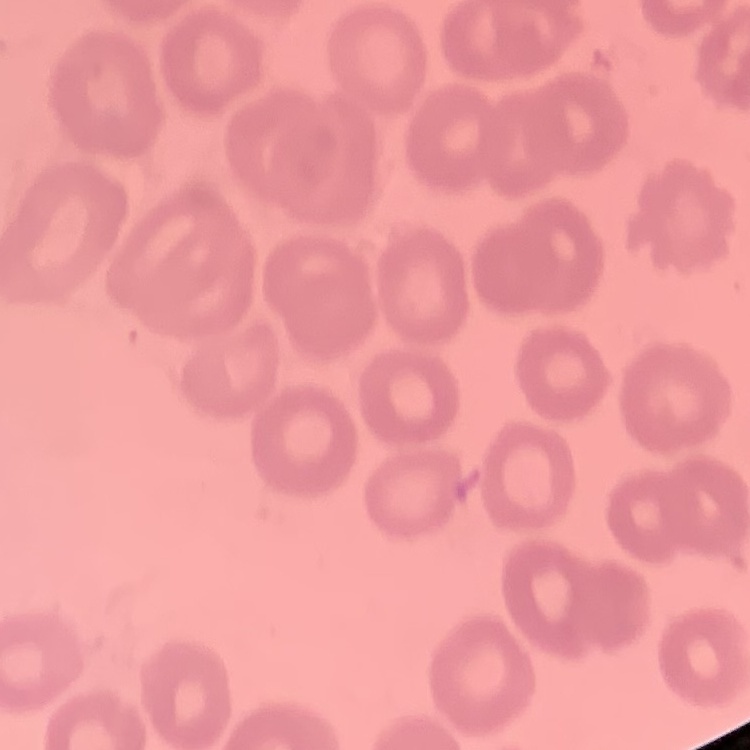
Summary:
  - Erythrocyte morphology: no rouleaux formation
  - Stain: Field's or Giemsa
  - Preparation: thin blood film
  - Image type: one tile cut from a larger photomicrograph